Identify the blood parasite species.
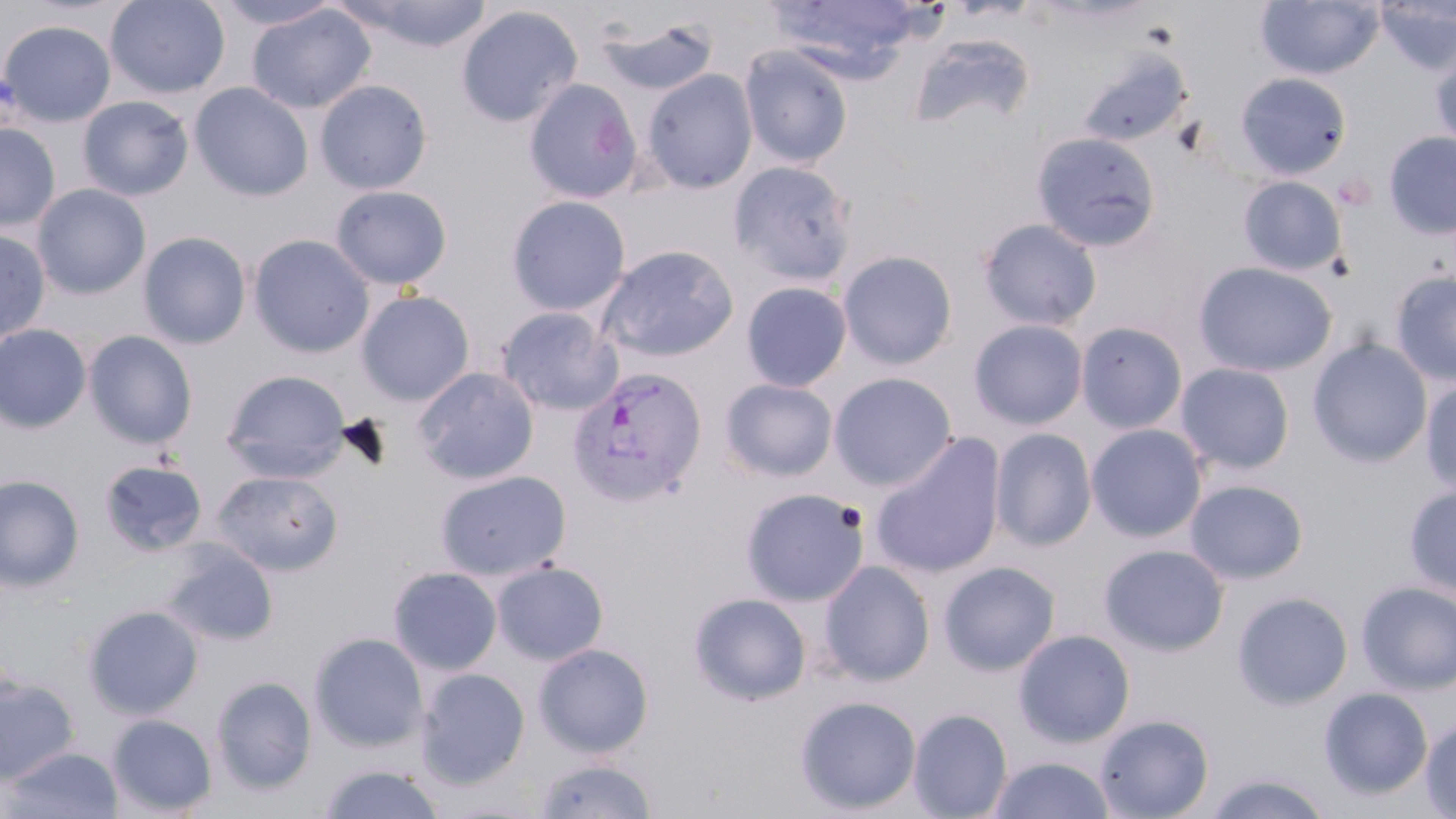

Plasmodium vivax.

magnification = 1000x
Plasmodium vivax-infected red blood cell locations = approximate bounding boxes as (x1,y1)-(x2,y2) corner pairs in pixels: (567,367)-(708,507)
stain = May-Grünwald-Giemsa
image size = 1456×819 pixels
field of view = single
modality = light microscopy
preparation = thin blood smear
uninfected red blood cell locations = approximate bounding boxes as (x1,y1)-(x2,y2) corner pairs in pixels: (105,0)-(230,99), (210,0)-(343,30), (338,0)-(495,53), (766,0)-(924,78), (1256,0)-(1384,80), (1375,2)-(1456,76), (246,4)-(376,114), (455,5)-(584,128), (596,16)-(719,97), (0,20)-(116,126), (907,31)-(1037,135), (739,44)-(853,169), (1430,47)-(1456,153), (1076,51)-(1190,149), (642,69)-(757,194), (1235,72)-(1351,179), (524,78)-(641,204), (315,80)-(432,195), (190,82)-(314,202), (77,96)-(193,201), (0,122)-(60,232), (1031,131)-(1162,252), (1384,131)-(1456,239), (728,159)-(858,286), (1238,176)-(1346,276), (32,183)-(151,300), (330,184)-(453,289), (506,195)-(631,316), (977,218)-(1102,332), (0,228)-(51,343), (138,231)-(252,349), (247,234)-(376,358), (597,245)-(738,362), (837,249)-(958,370), (1194,261)-(1338,377), (1391,270)-(1456,388), (741,280)-(852,392), (356,290)-(476,406), (495,306)-(624,416), (968,318)-(1089,430), (1075,320)-(1188,435), (0,324)-(92,433), (83,330)-(198,450), (1308,337)-(1433,469), (1175,362)-(1296,475), (412,366)-(539,485), (221,369)-(351,481), (828,372)-(957,490), (718,377)-(838,482), (1420,377)-(1456,495), (1086,424)-(1208,542), (990,427)-(1097,551), (870,434)-(1006,580), (98,458)-(208,557), (212,469)-(343,575), (435,469)-(573,581), (0,474)-(85,591), (1185,479)-(1309,583), (1404,484)-(1456,600), (740,487)-(870,606), (163,541)-(278,647), (1099,543)-(1229,656), (819,560)-(936,686), (938,560)-(1061,676), (491,561)-(609,665), (388,566)-(503,675), (1356,581)-(1456,693), (1232,591)-(1354,709), (688,592)-(812,705), (83,604)-(204,720), (1013,628)-(1136,747), (309,632)-(429,752), (533,643)-(655,758), (415,668)-(530,789), (0,674)-(81,783), (211,676)-(317,795), (1319,687)-(1433,800), (794,695)-(922,814), (908,708)-(1013,819), (1094,713)-(1214,819), (107,714)-(217,817), (1420,719)-(1456,817), (3,746)-(122,819), (988,756)-(1115,818), (532,758)-(658,819), (319,763)-(446,819), (1202,771)-(1335,819)